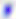
Summary:
  - Identification: Toxoplasma gondii
  - Modality: photomicrograph
  - Magnification: 400x